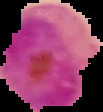 Image is 103×112 pixels. From a thin blood film. Malaria status: parasitized. Segmented cell region on a black background.